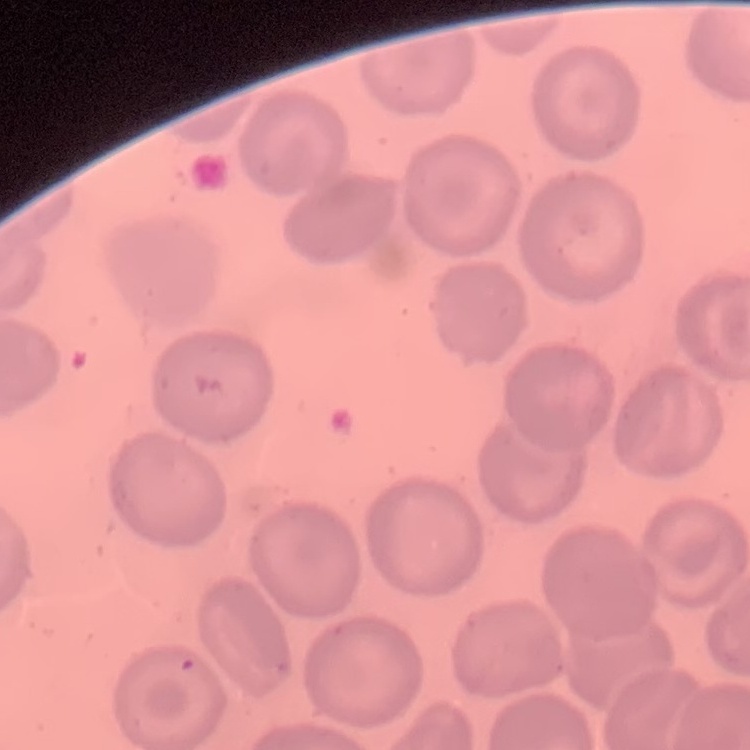
The erythrocytes exhibit no rouleaux formation. Thin peripheral smear. One tile cut from a larger photomicrograph. Field's or Giemsa stain.